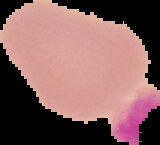

Summary:
  - Preparation: thin blood smear
  - Malaria status: uninfected
  - Image size: 160×145 pixels
  - Image type: segmented cell region with the area outside set to black